Identify the parasite.
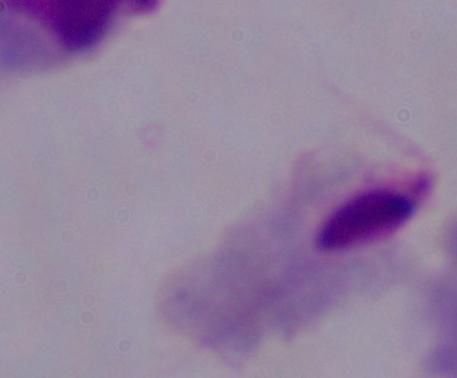

This is a trichomonad.

Captured at 1000x magnification. Micrograph.